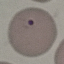 Malaria status: uninfected. Giemsa stain. Cell patch, automatically extracted from a larger field of view and resized to 64 × 64 pixels. Acquired by smartphone through the microscope eyepiece. Thin blood smear.